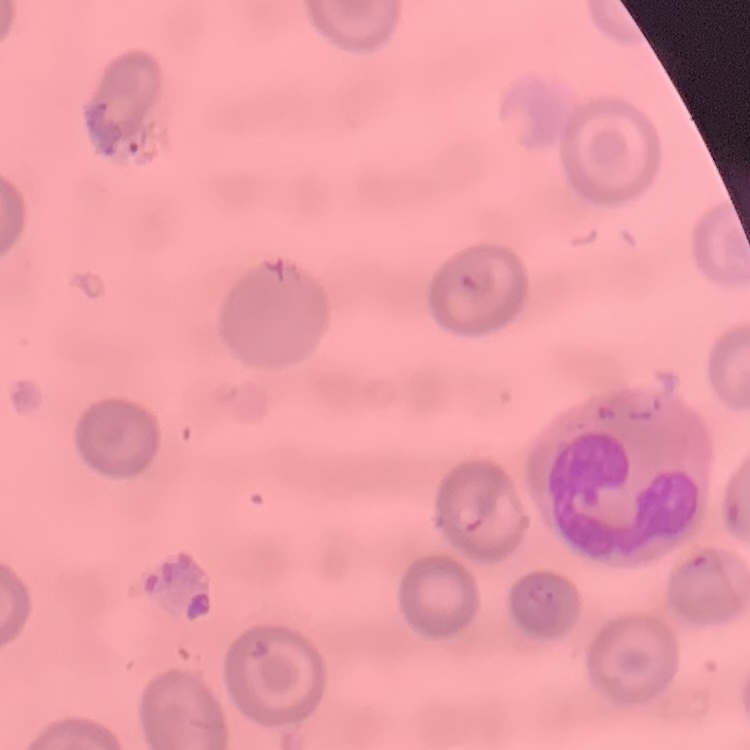
erythrocyte morphology = no rouleaux formation
image type = one tile cut from a larger photomicrograph
stain = Field's or Giemsa
preparation = thin peripheral smear